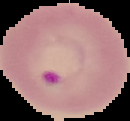
Summary:
  - Image type: segmented cell region with the area outside set to black
  - Image size: 130×121 pixels
  - Result: malaria parasites identified
  - Preparation: thin blood film